Outline each blood parasite and name the species.
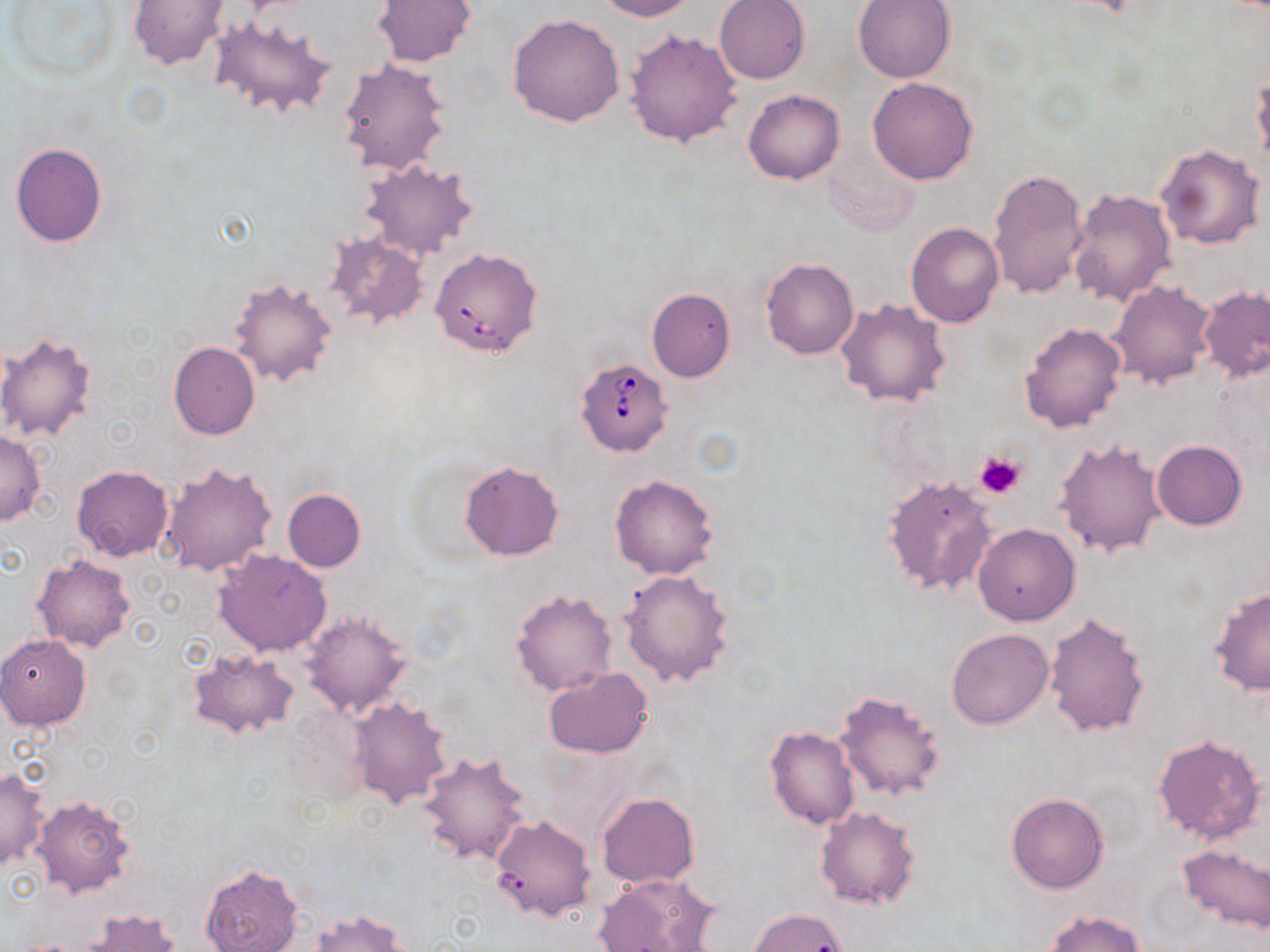

Approximate bounding boxes as [x1, y1, x2, y2] in pixels.
Babesia divergens-infected red blood cells: [436, 251, 546, 359], [576, 357, 673, 457].
No Plasmodium falciparum, Plasmodium ovale, Plasmodium malariae, Plasmodium vivax, or Trypanosoma brucei observed.

slide_level_diagnosis: Babesia divergens
preparation: thin blood smear
image_size: 1270×952 pixels
modality: optical microscopy
platelet_locations: 'approximate bounding boxes as [x1, y1, x2, y2] in pixels: [974, 449, 1027, 500]'
uninfected_red_blood_cell_locations: 'approximate bounding boxes as [x1, y1, x2, y2] in pixels: [128, 0, 231, 69], [371, 0, 479, 68], [593, 0, 698, 21], [853, 0, 957, 83], [4, 1, 120, 83], [715, 1, 810, 84], [507, 13, 625, 128], [208, 16, 338, 122], [624, 28, 744, 149], [338, 58, 451, 176], [868, 76, 977, 184], [1252, 76, 1270, 173], [744, 89, 844, 184], [10, 141, 108, 247], [1156, 143, 1265, 250], [360, 159, 479, 262], [988, 169, 1088, 299], [1066, 188, 1176, 309], [907, 222, 1004, 328], [324, 231, 429, 329], [761, 259, 860, 360], [228, 277, 338, 386], [1109, 280, 1217, 389], [645, 286, 736, 383], [1199, 287, 1270, 381], [835, 297, 952, 408], [1019, 321, 1127, 432], [0, 332, 100, 442], [169, 341, 260, 440], [0, 430, 45, 526], [1055, 437, 1166, 559], [1152, 440, 1248, 530], [460, 460, 564, 561], [159, 461, 275, 577], [72, 464, 173, 561], [609, 474, 718, 579], [882, 475, 999, 597], [282, 489, 366, 572], [972, 523, 1080, 626], [213, 548, 332, 657], [32, 554, 135, 652], [619, 568, 734, 687], [1208, 586, 1269, 698], [511, 588, 619, 696], [301, 609, 412, 719], [1043, 613, 1151, 738], [946, 628, 1054, 729], [0, 634, 92, 730], [188, 648, 300, 739], [543, 668, 654, 757], [833, 689, 948, 802], [347, 697, 452, 810], [282, 706, 372, 811], [764, 726, 860, 830], [1152, 732, 1265, 845], [418, 751, 532, 866], [1, 767, 49, 871], [596, 791, 699, 887], [1006, 792, 1108, 893], [32, 795, 136, 898], [815, 806, 921, 910], [489, 814, 597, 922], [1178, 844, 1270, 933], [199, 864, 302, 952], [594, 872, 719, 952], [307, 908, 411, 952], [750, 908, 850, 952], [80, 909, 181, 952], [1043, 909, 1145, 952]'
field_of_view: one of a larger specimen
stain: May-Grünwald-Giemsa
magnification: 1000x